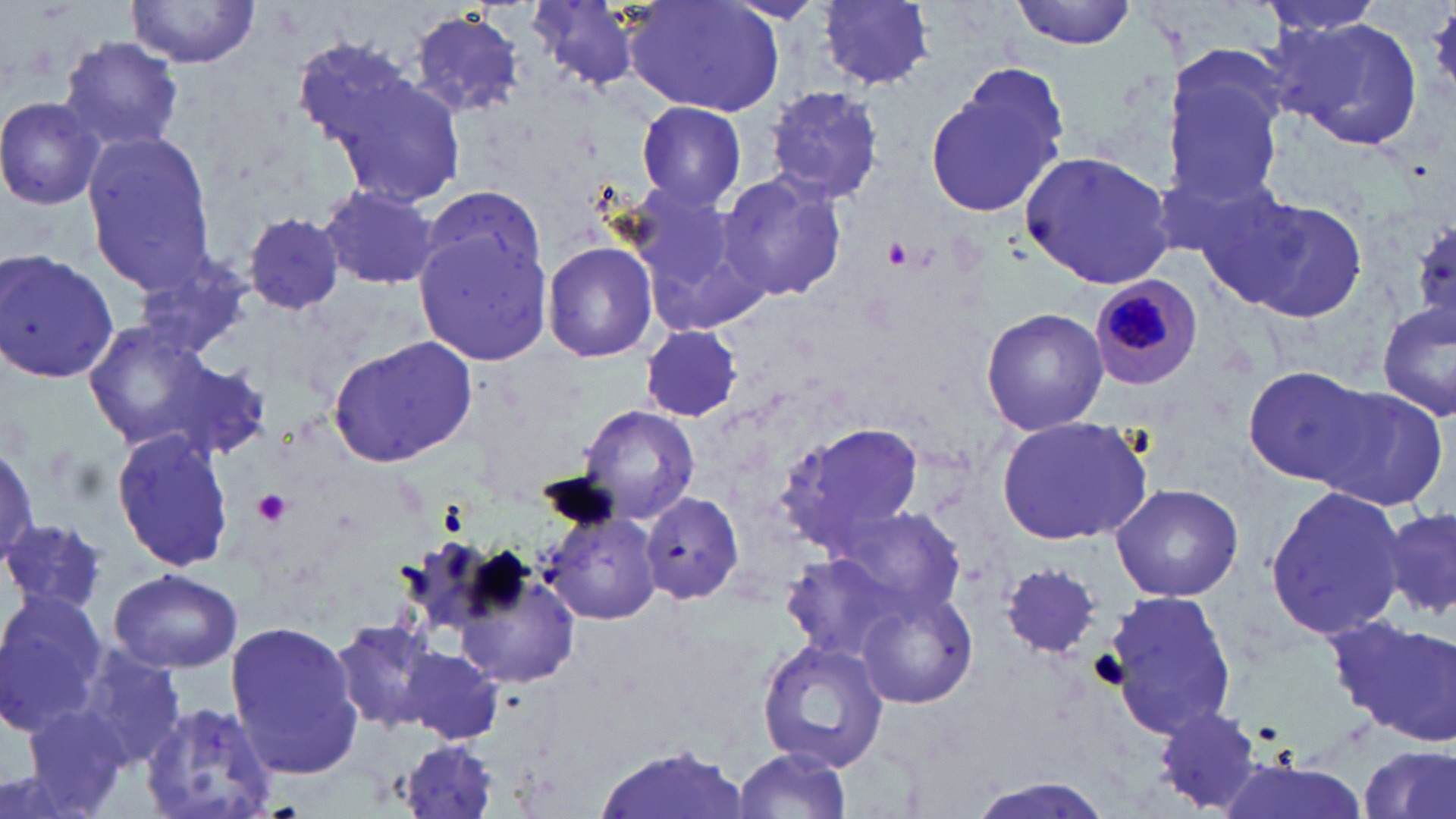
slide-level diagnosis = Plasmodium malariae
magnification = 1000x
uninfected red blood cell locations = approximate bounding boxes as [x1, y1, x2, y2] in pixels: [525, 0, 642, 90], [626, 0, 786, 116], [819, 0, 935, 89], [1010, 0, 1137, 49], [1256, 0, 1390, 38], [129, 1, 259, 68], [406, 11, 528, 120], [1279, 18, 1425, 149], [58, 34, 187, 153], [290, 35, 418, 148], [1163, 54, 1287, 209], [925, 67, 1068, 220], [329, 70, 465, 206], [764, 87, 887, 203], [0, 95, 106, 209], [637, 101, 747, 211], [81, 133, 220, 293], [1020, 150, 1177, 288], [717, 169, 847, 303], [624, 184, 766, 323], [317, 185, 443, 291], [416, 186, 547, 290], [1218, 192, 1373, 323], [243, 213, 346, 315], [413, 228, 551, 368], [542, 240, 659, 362], [0, 248, 120, 388], [131, 248, 252, 359], [1378, 302, 1456, 423], [980, 307, 1108, 433], [82, 320, 221, 449], [637, 327, 745, 421], [328, 336, 480, 469], [153, 358, 271, 463], [1242, 366, 1374, 485], [1311, 386, 1452, 510], [576, 403, 700, 526], [994, 415, 1152, 545], [779, 422, 923, 549], [113, 428, 232, 574], [0, 442, 39, 569], [1110, 483, 1243, 602], [1264, 485, 1405, 643], [639, 492, 746, 605], [831, 506, 969, 622], [538, 508, 664, 627], [1376, 510, 1456, 618], [2, 517, 104, 616], [781, 556, 902, 660], [456, 561, 583, 690], [1002, 563, 1102, 660], [109, 567, 243, 673], [854, 585, 979, 709], [1102, 588, 1239, 736], [0, 589, 109, 733], [1328, 614, 1454, 742], [331, 616, 444, 731], [227, 621, 366, 777], [758, 638, 888, 772], [400, 644, 503, 744], [69, 646, 188, 768], [140, 702, 279, 819], [1152, 705, 1264, 814], [19, 708, 140, 819], [397, 739, 502, 819], [600, 745, 749, 819], [1359, 747, 1455, 819], [730, 749, 853, 818], [1212, 759, 1369, 819], [960, 777, 1121, 819]
preparation = thin blood film
modality = optical microscopy
platelet locations = approximate bounding boxes as [x1, y1, x2, y2] in pixels: [1427, 8, 1456, 91], [881, 235, 917, 270], [254, 490, 292, 527], [1089, 650, 1129, 691]
stain = May-Grünwald-Giemsa
Plasmodium malariae-infected red blood cell locations = approximate bounding boxes as [x1, y1, x2, y2] in pixels: [1089, 276, 1201, 390]
image size = 1456×819 pixels
field of view = single